Identify the parasite.
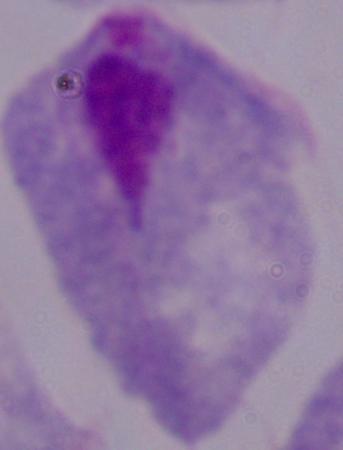

This is a trichomonad.

Summary:
  - Modality: micrograph
  - Magnification: 1000x